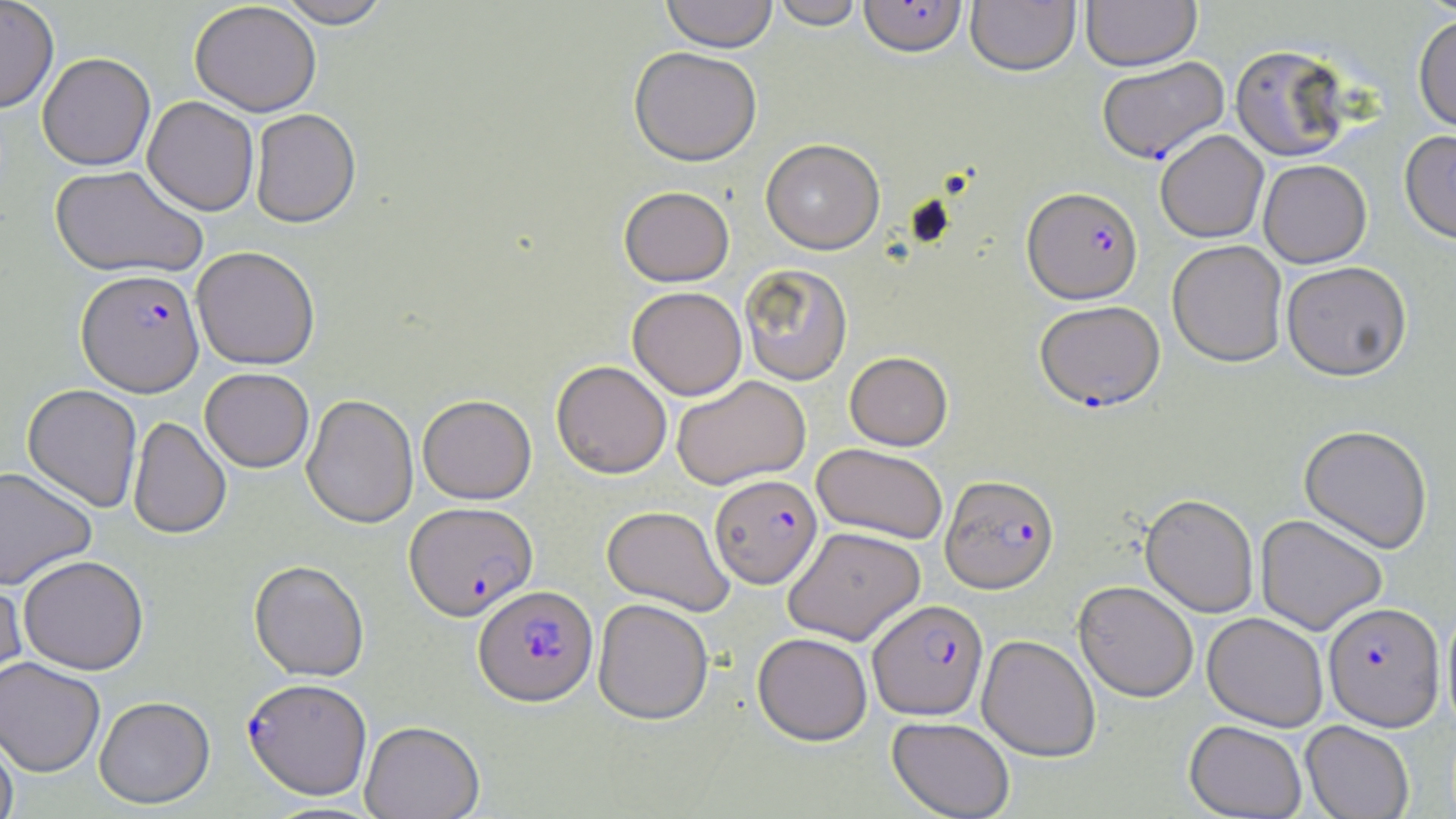
Summary:
  - Coordinate format: approximate bounding boxes as (x1, y1, x2, y2) in pixels
  - Plasmodium falciparum-infected red blood cell locations: (858, 0, 967, 57), (1098, 55, 1231, 162), (1023, 186, 1142, 304), (77, 269, 204, 396), (1035, 300, 1166, 411), (710, 473, 822, 589), (940, 474, 1059, 593), (404, 501, 538, 620), (474, 585, 598, 705), (868, 599, 988, 720), (1323, 602, 1444, 729), (243, 678, 372, 800)
  - Uninfected red blood cell locations: (0, 0, 59, 112), (275, 0, 393, 28), (661, 0, 778, 52), (770, 0, 866, 29), (1081, 0, 1201, 71), (189, 1, 321, 116), (966, 1, 1080, 76), (1413, 13, 1456, 134), (1230, 44, 1353, 162), (629, 46, 762, 166), (37, 52, 155, 170), (142, 96, 259, 215), (250, 108, 361, 227), (1400, 129, 1456, 245), (1155, 130, 1269, 243), (761, 138, 884, 254), (1258, 159, 1372, 268), (50, 164, 208, 279), (619, 186, 734, 286), (1167, 239, 1288, 367), (192, 246, 320, 370), (1281, 261, 1412, 380), (739, 263, 853, 385), (628, 286, 747, 400), (844, 351, 953, 451), (551, 360, 672, 478), (200, 368, 314, 472), (671, 375, 810, 490), (22, 384, 143, 512), (301, 394, 418, 528), (417, 394, 537, 504), (127, 417, 231, 539), (1299, 424, 1433, 553), (811, 443, 948, 544), (0, 467, 97, 590), (1141, 493, 1259, 617), (602, 505, 735, 616), (1255, 513, 1388, 635), (783, 525, 926, 645), (18, 555, 149, 675), (249, 560, 369, 682), (0, 574, 28, 697), (1073, 580, 1199, 702), (593, 598, 714, 724), (1442, 602, 1456, 735), (1202, 612, 1328, 731), (752, 632, 872, 745), (977, 635, 1101, 761), (0, 656, 105, 777), (94, 696, 215, 809), (887, 716, 1015, 819), (360, 720, 485, 819), (1184, 720, 1307, 818), (1300, 720, 1415, 819), (0, 732, 19, 819)
  - Slide-level diagnosis: Plasmodium falciparum
  - Magnification: 1000x
  - Stain: May-Grünwald-Giemsa
  - Field of view: one of a larger specimen
  - Modality: optical microscopy
  - Preparation: thin blood film
  - Image size: 1456×819 pixels